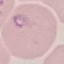 Malaria status: parasitized. Thin blood film. Giemsa-stained preparation. Cell patch, automatically extracted from a larger field of view and resized to 64 × 64 pixels. Acquired by smartphone through the microscope eyepiece.